Comment on the morphology of the red blood cells.
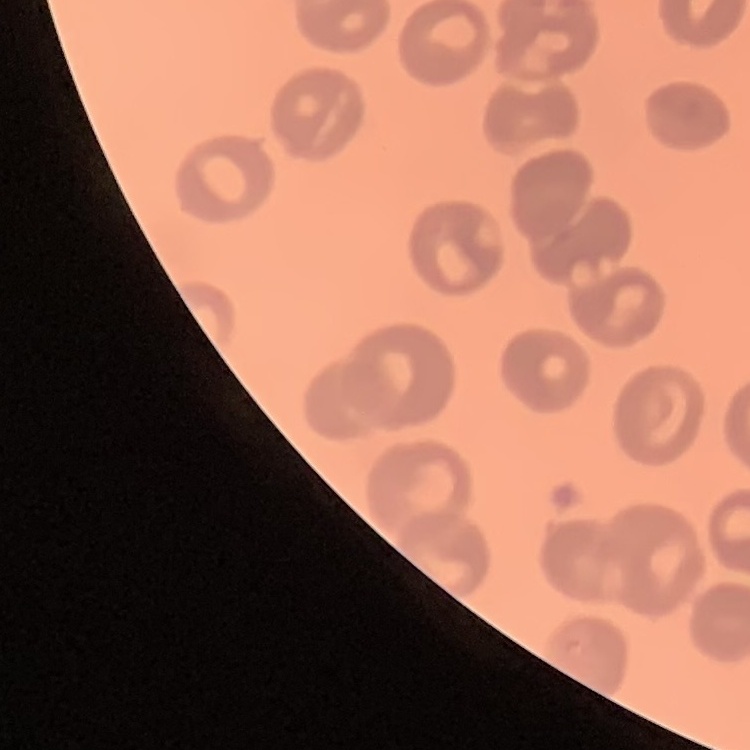
They show no rouleaux formation.

Square crop of a larger photomicrograph. Thin peripheral smear. Field's or Giemsa stain.